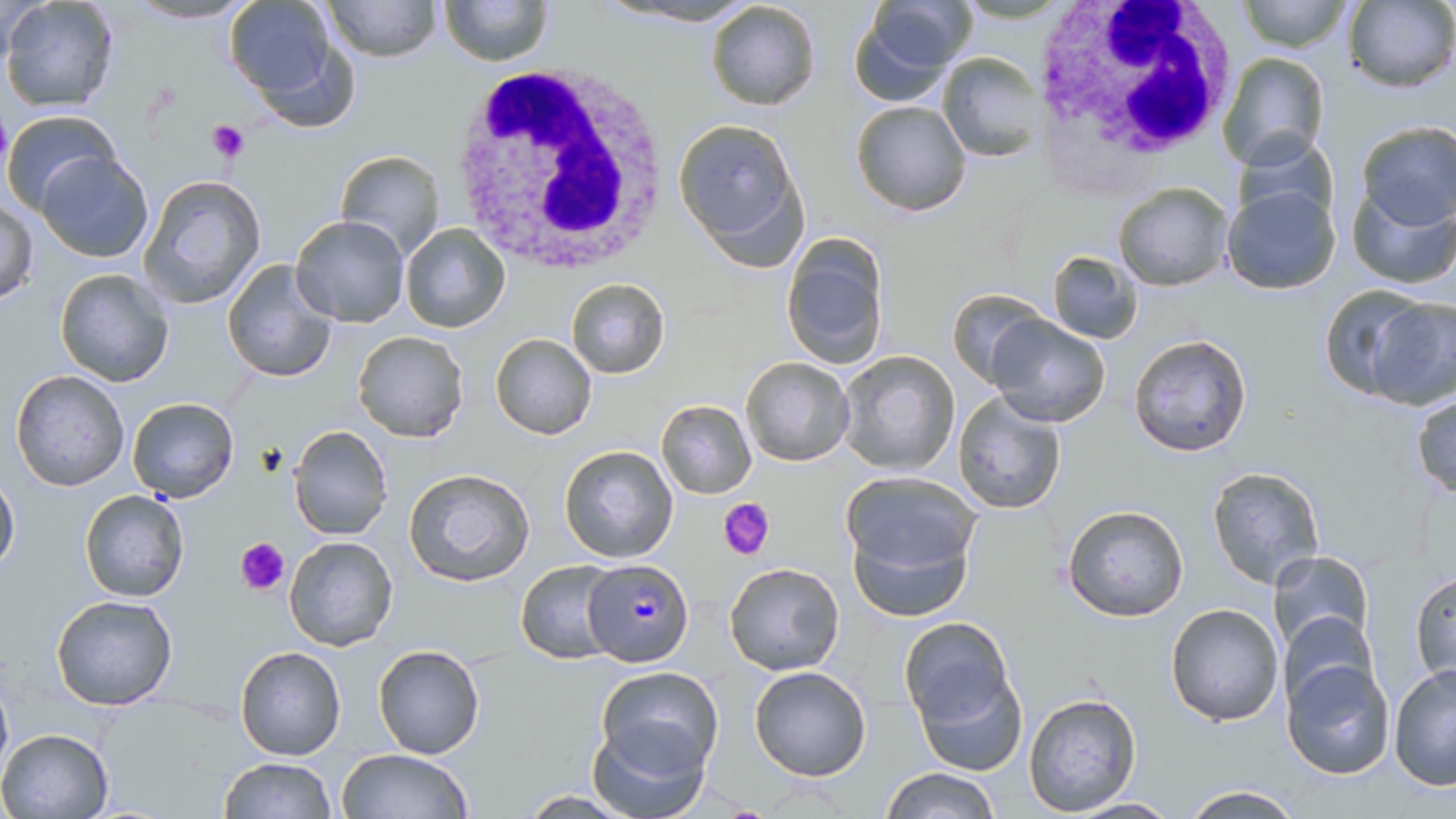

Approximate bounding boxes as named x1/y1/x2/y2 corners in pixels. White blood cell locations: (x1=1027, y1=0, x2=1236, y2=178), (x1=446, y1=60, x2=675, y2=272). Platelet locations: (x1=207, y1=121, x2=252, y2=163), (x1=719, y1=496, x2=777, y2=560), (x1=235, y1=535, x2=291, y2=595). Plasmodium falciparum-infected red blood cell locations: (x1=582, y1=559, x2=692, y2=667). Uninfected red blood cell locations: (x1=1, y1=0, x2=121, y2=114), (x1=123, y1=0, x2=259, y2=24), (x1=325, y1=0, x2=439, y2=62), (x1=440, y1=0, x2=552, y2=66), (x1=607, y1=0, x2=760, y2=26), (x1=850, y1=0, x2=974, y2=105), (x1=1236, y1=0, x2=1353, y2=52), (x1=1343, y1=0, x2=1456, y2=93), (x1=224, y1=1, x2=339, y2=99), (x1=704, y1=1, x2=821, y2=113), (x1=936, y1=52, x2=1045, y2=162), (x1=1217, y1=52, x2=1329, y2=170), (x1=851, y1=100, x2=972, y2=217), (x1=2, y1=109, x2=122, y2=213), (x1=673, y1=116, x2=803, y2=259), (x1=1355, y1=121, x2=1456, y2=230), (x1=1235, y1=131, x2=1337, y2=227), (x1=335, y1=148, x2=446, y2=258), (x1=38, y1=152, x2=154, y2=263), (x1=139, y1=174, x2=267, y2=309), (x1=1112, y1=182, x2=1234, y2=292), (x1=1346, y1=182, x2=1456, y2=291), (x1=1221, y1=185, x2=1341, y2=297), (x1=1, y1=199, x2=38, y2=305), (x1=289, y1=215, x2=411, y2=327), (x1=401, y1=223, x2=510, y2=334), (x1=780, y1=234, x2=889, y2=370), (x1=1046, y1=249, x2=1143, y2=344), (x1=222, y1=259, x2=342, y2=385), (x1=54, y1=267, x2=175, y2=386), (x1=565, y1=277, x2=671, y2=379), (x1=1318, y1=285, x2=1435, y2=398), (x1=945, y1=291, x2=1049, y2=388), (x1=1364, y1=298, x2=1454, y2=411), (x1=986, y1=313, x2=1112, y2=427), (x1=352, y1=330, x2=469, y2=443), (x1=490, y1=333, x2=596, y2=440), (x1=1128, y1=334, x2=1254, y2=458), (x1=838, y1=349, x2=960, y2=475), (x1=740, y1=356, x2=854, y2=467), (x1=9, y1=369, x2=129, y2=493), (x1=660, y1=384, x2=830, y2=488), (x1=1411, y1=391, x2=1456, y2=501), (x1=953, y1=393, x2=1067, y2=515), (x1=127, y1=396, x2=239, y2=504), (x1=656, y1=399, x2=757, y2=498), (x1=286, y1=426, x2=392, y2=542), (x1=558, y1=444, x2=679, y2=563), (x1=1207, y1=466, x2=1325, y2=588), (x1=402, y1=467, x2=535, y2=590), (x1=0, y1=471, x2=19, y2=575), (x1=844, y1=481, x2=980, y2=621), (x1=80, y1=489, x2=189, y2=602), (x1=1061, y1=503, x2=1189, y2=623), (x1=283, y1=536, x2=398, y2=652), (x1=1268, y1=550, x2=1373, y2=661), (x1=515, y1=560, x2=622, y2=665), (x1=724, y1=562, x2=847, y2=676), (x1=1411, y1=570, x2=1455, y2=684), (x1=51, y1=595, x2=179, y2=710), (x1=1165, y1=602, x2=1284, y2=727), (x1=1279, y1=609, x2=1377, y2=713), (x1=900, y1=618, x2=1011, y2=729), (x1=234, y1=644, x2=346, y2=761), (x1=372, y1=645, x2=485, y2=761), (x1=1282, y1=657, x2=1397, y2=778), (x1=1388, y1=663, x2=1456, y2=791), (x1=0, y1=666, x2=13, y2=788), (x1=748, y1=666, x2=871, y2=781), (x1=910, y1=666, x2=1028, y2=777), (x1=596, y1=667, x2=724, y2=774), (x1=1023, y1=692, x2=1144, y2=817), (x1=585, y1=716, x2=711, y2=819), (x1=0, y1=727, x2=113, y2=818), (x1=334, y1=749, x2=475, y2=819), (x1=219, y1=757, x2=337, y2=818), (x1=880, y1=766, x2=999, y2=819), (x1=1178, y1=785, x2=1306, y2=818), (x1=517, y1=790, x2=643, y2=817), (x1=1066, y1=796, x2=1183, y2=817). Slide-level diagnosis: Plasmodium falciparum. 1000x magnification. Single field of view. Light microscopy. May-Grünwald-Giemsa stain. Image is 1456×819 pixels. Thin blood film.